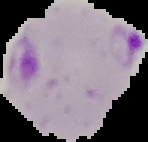 The area outside the segmented cell region is set to black. Image is 148×142 pixels. Malaria status: parasitized. From a thin blood film.